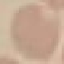
Summary:
  - Malaria status: uninfected
  - Preparation: thin smear
  - Capture: smartphone camera at the microscope eyepiece
  - Image type: automatically extracted cell patch, resized to 64 × 64 pixels
  - Stain: Giemsa